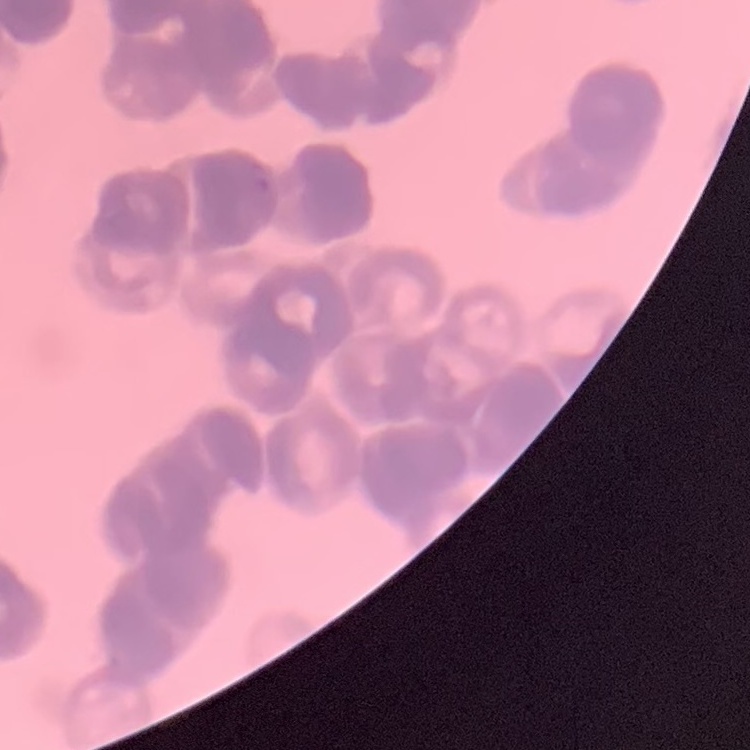
The red blood cells exhibit rouleaux formation. Square crop of a larger photomicrograph. Field's or Giemsa stain. Thin peripheral smear.